State the blood parasite species.
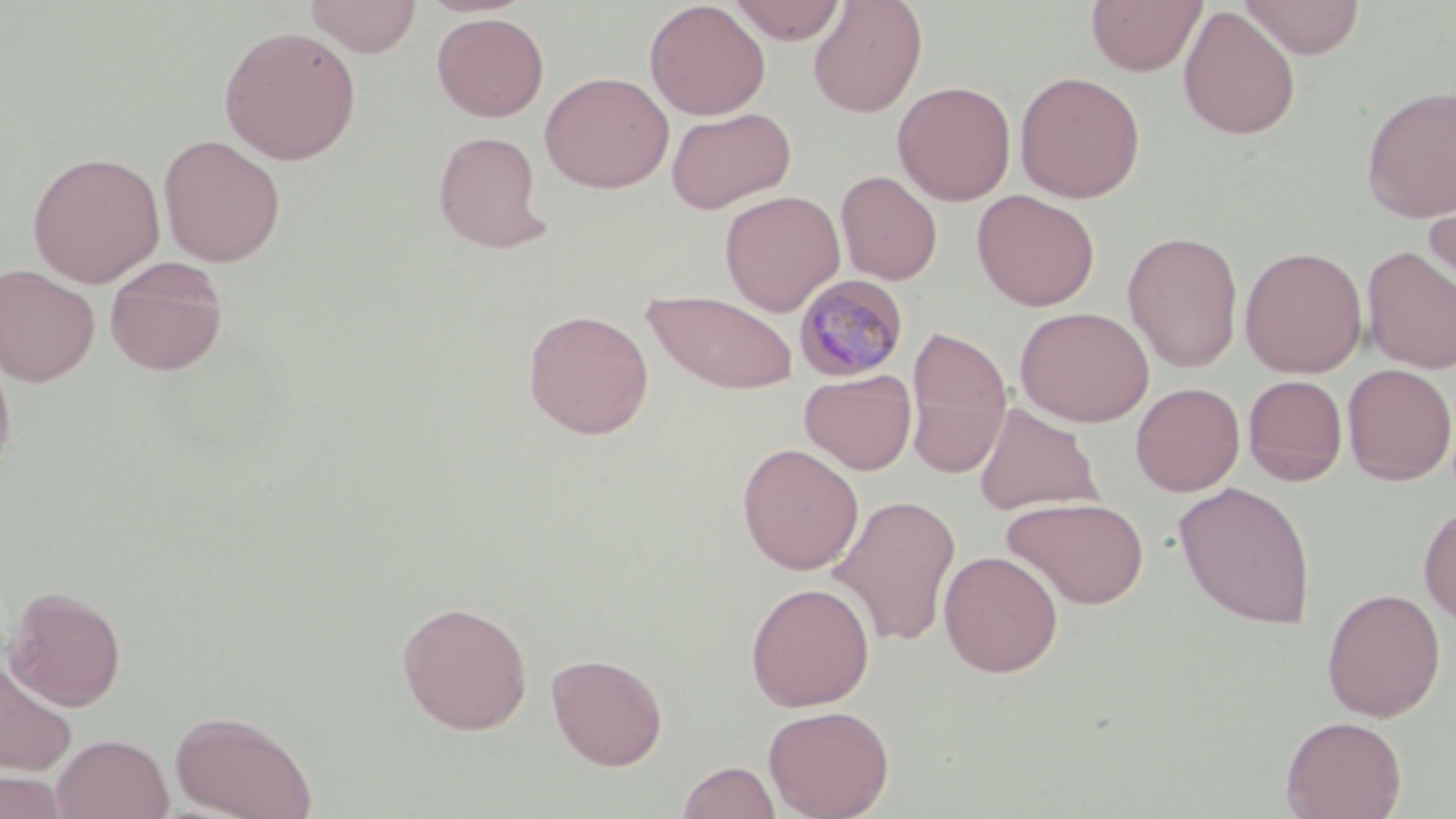

Plasmodium malariae.

Summary:
  - Coordinate format: approximate bounding boxes as named x1/y1/x2/y2 corners in pixels
  - Uninfected red blood cell locations: (x1=304, y1=0, x2=423, y2=57), (x1=644, y1=0, x2=770, y2=120), (x1=808, y1=0, x2=928, y2=117), (x1=1086, y1=0, x2=1207, y2=76), (x1=1239, y1=0, x2=1366, y2=58), (x1=728, y1=1, x2=848, y2=45), (x1=1178, y1=6, x2=1301, y2=141), (x1=431, y1=12, x2=549, y2=122), (x1=218, y1=25, x2=362, y2=165), (x1=1013, y1=70, x2=1146, y2=203), (x1=539, y1=71, x2=674, y2=193), (x1=892, y1=80, x2=1016, y2=205), (x1=1360, y1=85, x2=1456, y2=223), (x1=665, y1=106, x2=796, y2=214), (x1=432, y1=130, x2=552, y2=254), (x1=158, y1=134, x2=286, y2=267), (x1=27, y1=151, x2=165, y2=288), (x1=835, y1=170, x2=942, y2=286), (x1=1422, y1=174, x2=1456, y2=305), (x1=971, y1=189, x2=1100, y2=311), (x1=720, y1=190, x2=845, y2=316), (x1=1122, y1=230, x2=1244, y2=372), (x1=1239, y1=245, x2=1368, y2=378), (x1=1361, y1=245, x2=1456, y2=374), (x1=104, y1=257, x2=229, y2=376), (x1=0, y1=264, x2=100, y2=387), (x1=642, y1=289, x2=799, y2=394), (x1=1015, y1=307, x2=1154, y2=427), (x1=522, y1=308, x2=655, y2=439), (x1=905, y1=325, x2=1012, y2=478), (x1=0, y1=336, x2=17, y2=474), (x1=1341, y1=363, x2=1455, y2=484), (x1=799, y1=369, x2=917, y2=474), (x1=1242, y1=374, x2=1348, y2=485), (x1=1130, y1=382, x2=1245, y2=496), (x1=973, y1=402, x2=1102, y2=516), (x1=737, y1=442, x2=864, y2=575), (x1=1173, y1=481, x2=1317, y2=629), (x1=829, y1=494, x2=962, y2=647), (x1=1002, y1=496, x2=1150, y2=609), (x1=1418, y1=503, x2=1456, y2=626), (x1=938, y1=550, x2=1063, y2=677), (x1=745, y1=581, x2=875, y2=711), (x1=4, y1=585, x2=127, y2=711), (x1=1321, y1=587, x2=1446, y2=722), (x1=396, y1=600, x2=533, y2=735), (x1=547, y1=652, x2=668, y2=770), (x1=0, y1=660, x2=78, y2=775), (x1=763, y1=704, x2=895, y2=819), (x1=171, y1=710, x2=318, y2=819), (x1=1280, y1=715, x2=1407, y2=819), (x1=51, y1=733, x2=174, y2=819), (x1=677, y1=761, x2=781, y2=819), (x1=0, y1=768, x2=71, y2=818)
  - Plasmodium malariae-infected red blood cell locations: (x1=793, y1=273, x2=910, y2=382)
  - Magnification: 1000x
  - Field of view: single
  - Modality: optical microscopy
  - Preparation: thin blood smear
  - Stain: May-Grünwald-Giemsa
  - Image size: 1456×819 pixels